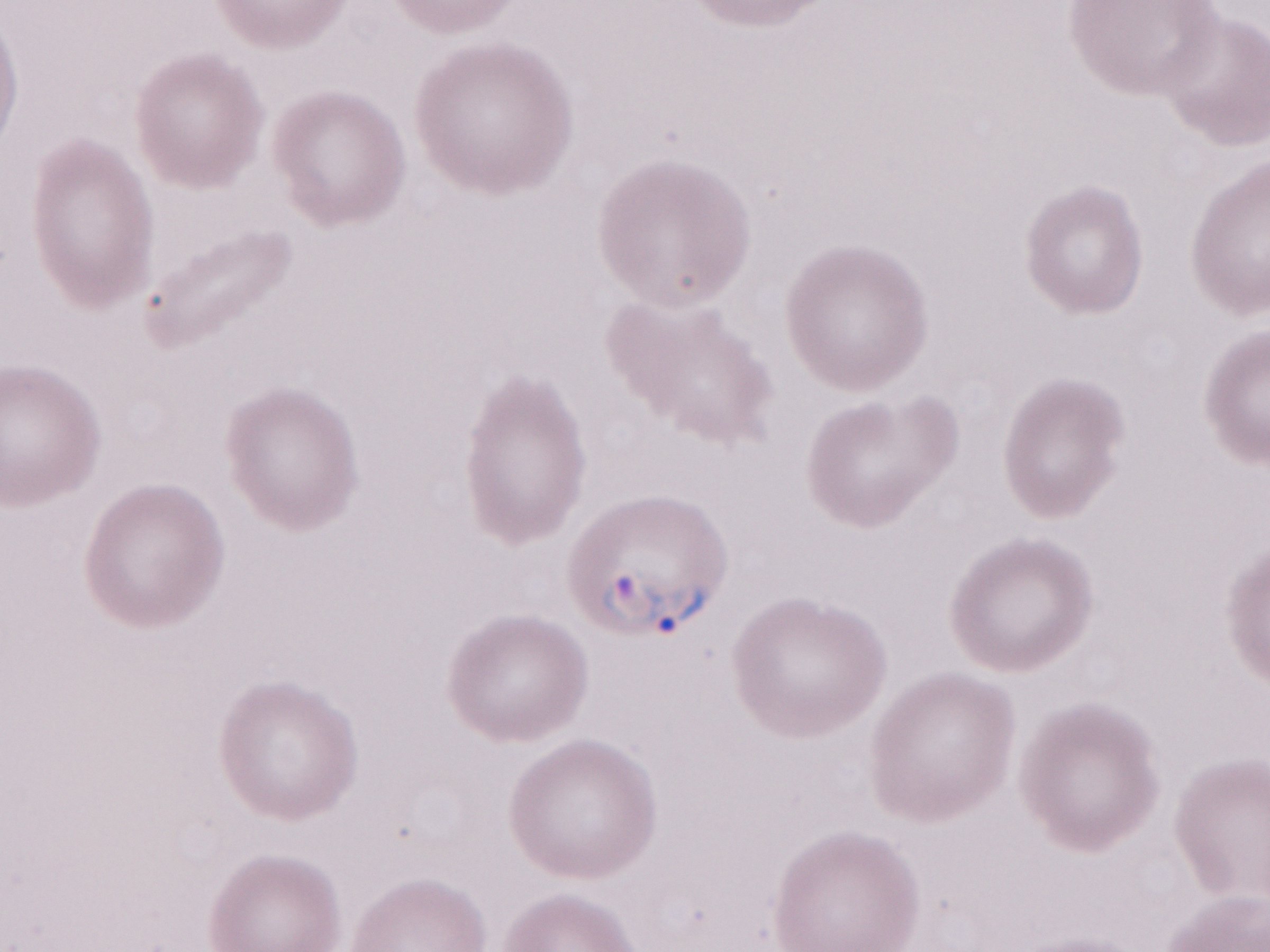 Magnification: 1,000x. One field of this slide. May-Grünwald-Giemsa-stained preparation. Malaria diagnosis (patient-level): positive. Image is 1270×952 pixels. Thin blood film. Olympus BX43 microscope and DP73 digital camera.